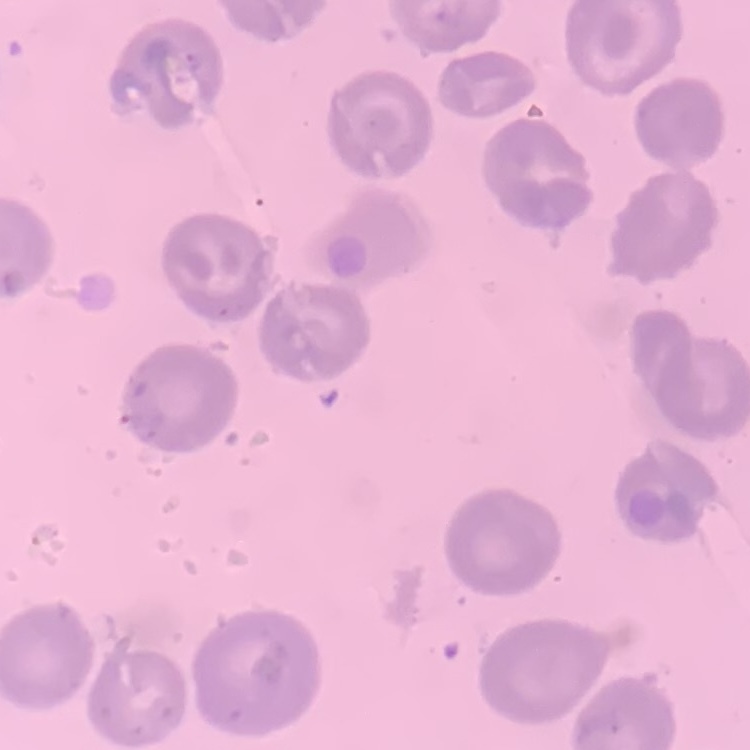

Summary:
  - Erythrocyte morphology: no rouleaux formation
  - Preparation: thin blood film
  - Image type: one tile cut from a larger photomicrograph
  - Stain: Field's or Giemsa